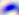
magnification = 400x
identification = Toxoplasma gondii
modality = photomicrograph